Identify the parasite.
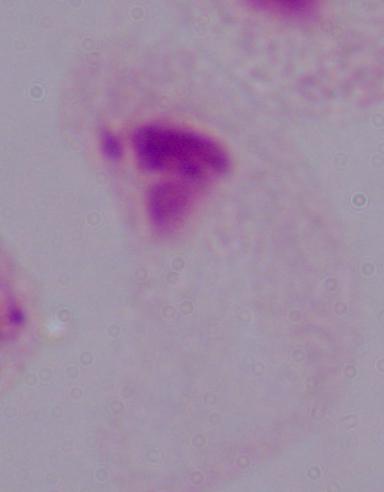
A trichomonad.

Summary:
  - Magnification: 1000x
  - Modality: photomicrograph